Name the parasite shown.
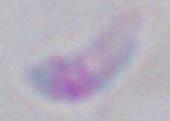

This is Toxoplasma gondii.

Micrograph. Captured at 1000x magnification.